Locate every Plasmodium parasite.
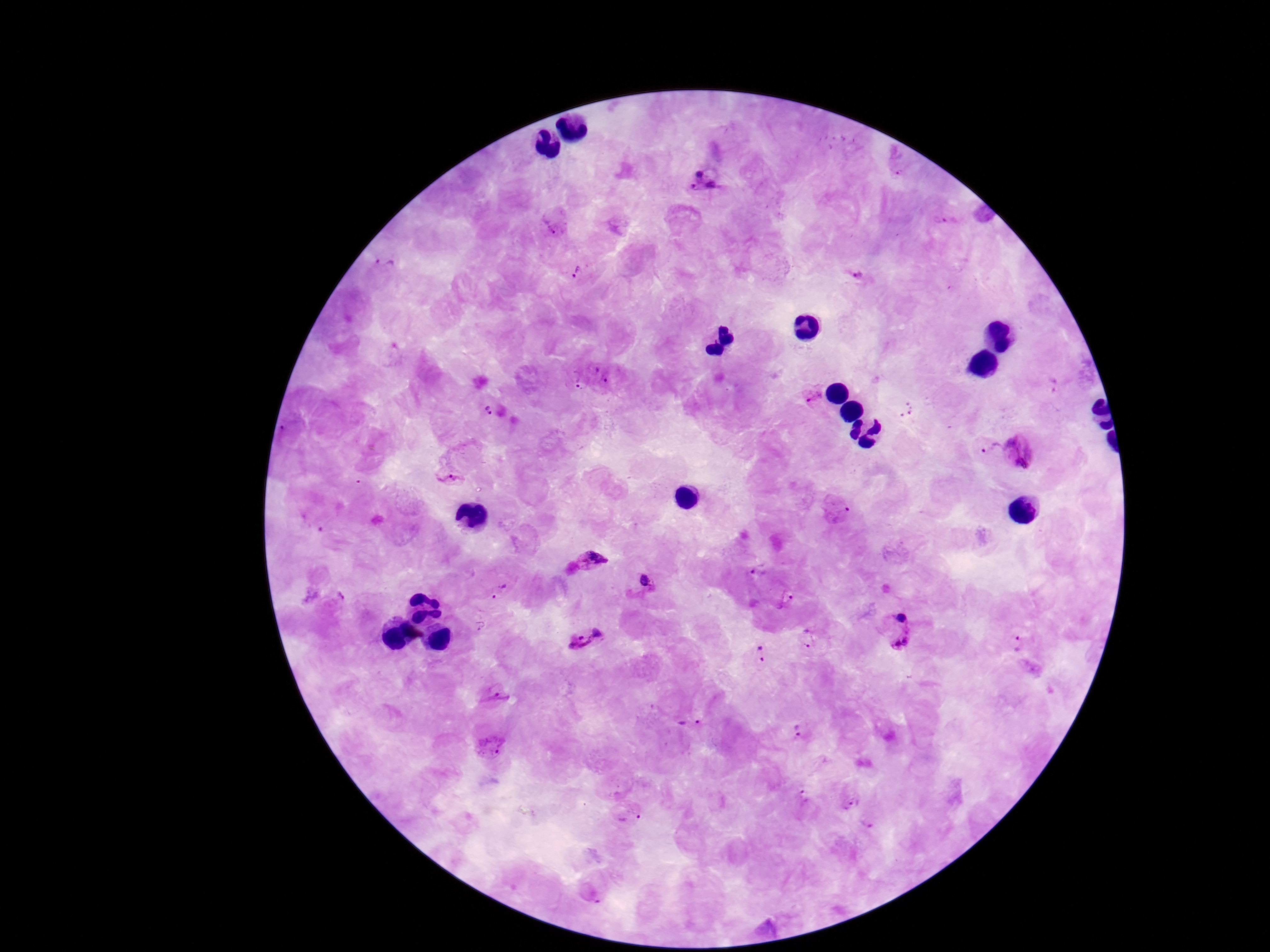
Approximate centers as {x, y} in pixels.
Plasmodium parasites: {903, 173}, {703, 180}, {943, 219}, {555, 223}, {386, 265}, {578, 269}, {858, 278}, {602, 373}, {575, 380}, {814, 396}, {492, 409}, {906, 409}, {985, 446}, {1021, 451}, {453, 477}, {589, 560}, {758, 570}, {649, 584}, {499, 589}, {340, 596}, {786, 598}, {899, 618}, {479, 626}, {807, 636}, {586, 637}, {902, 642}, {1018, 643}, {760, 654}, {492, 694}, {691, 724}, {799, 731}, {491, 745}, {803, 798}, {850, 802}, {628, 814}, {867, 825}.

Image is 1270×952 pixels. Thick blood smear. Smartphone photograph taken through the microscope eyepiece. Giemsa stain. Patient malaria status: infected. 100x magnification. Single field of view.